Comment on the morphology of the red blood cells.
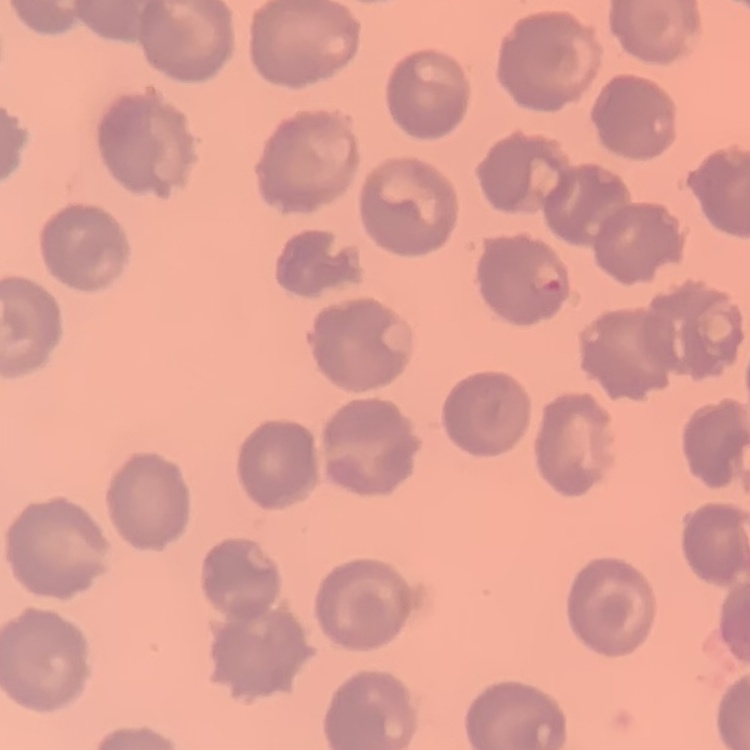

No rouleaux formation.

Summary:
  - Preparation: thin blood smear
  - Image type: one tile cut from a larger photomicrograph
  - Stain: Field's or Giemsa